Locate every blood parasite and identify its species.
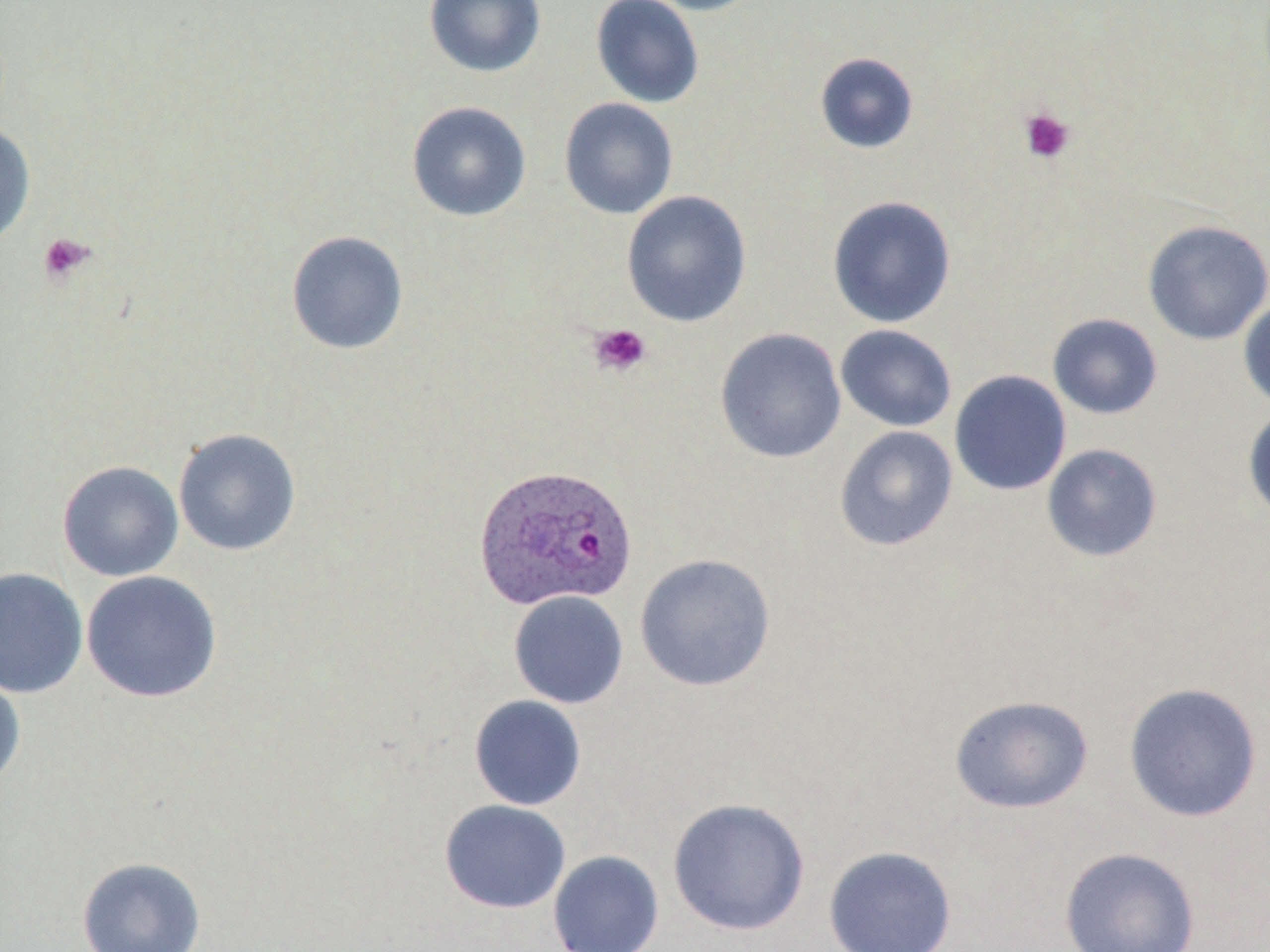
Approximate bounding boxes as (x1, y1, x2, y2) in pixels.
Plasmodium ovale-infected red blood cells: (473, 464, 638, 611).
No Plasmodium falciparum, Plasmodium malariae, Plasmodium vivax, Babesia divergens, or Trypanosoma brucei observed.

slide-level diagnosis = Plasmodium ovale
preparation = thin blood film
stain = May-Grünwald-Giemsa
image size = 1270×952 pixels
uninfected red blood cell locations = approximate bounding boxes as (x1, y1, x2, y2) in pixels: (424, 0, 546, 78), (590, 0, 705, 108), (641, 0, 766, 16), (814, 52, 920, 154), (559, 97, 679, 219), (406, 101, 531, 221), (0, 121, 36, 249), (621, 190, 753, 327), (827, 195, 957, 329), (1142, 219, 1270, 346), (286, 230, 409, 355), (1238, 297, 1270, 413), (1047, 313, 1163, 420), (835, 324, 957, 432), (714, 327, 847, 464), (949, 369, 1072, 496), (1243, 406, 1270, 526), (834, 425, 958, 552), (172, 427, 302, 556), (1041, 443, 1163, 562), (58, 460, 184, 582), (634, 553, 776, 692), (0, 567, 88, 698), (81, 570, 222, 703), (508, 590, 629, 709), (0, 671, 26, 791), (1123, 682, 1263, 823), (949, 694, 1094, 814), (468, 695, 587, 811), (667, 797, 810, 936), (439, 799, 571, 913), (823, 845, 957, 952), (1059, 847, 1201, 951), (548, 850, 664, 952), (77, 856, 206, 952)
magnification = 1000x
modality = optical microscopy
platelet locations = approximate bounding boxes as (x1, y1, x2, y2) in pixels: (1019, 106, 1076, 164), (38, 232, 95, 285), (587, 323, 652, 379)
field of view = one of a larger specimen